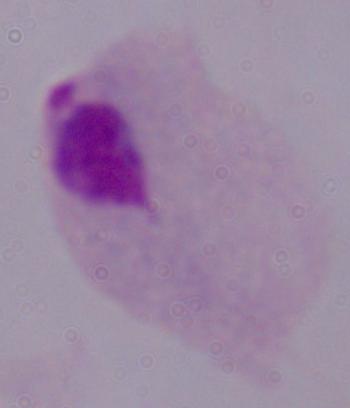
A trichomonad is shown. 1000x magnification. Photomicrograph.